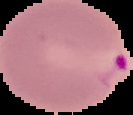

From a thin blood smear. Malaria status: parasitized. The area outside the segmented cell region is set to black. Image is 133×115 pixels.